Assess the morphology of the red blood cells.
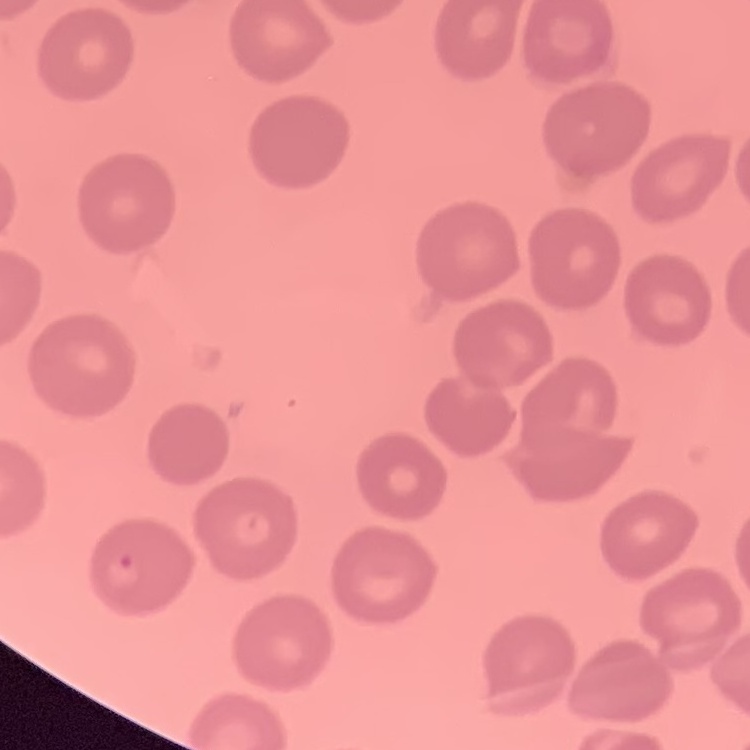

They show no rouleaux formation.

{
  "image_type": "one tile cut from a larger photomicrograph",
  "stain": "Field's or Giemsa",
  "preparation": "thin peripheral smear"
}